Locate every blood parasite and identify its species.
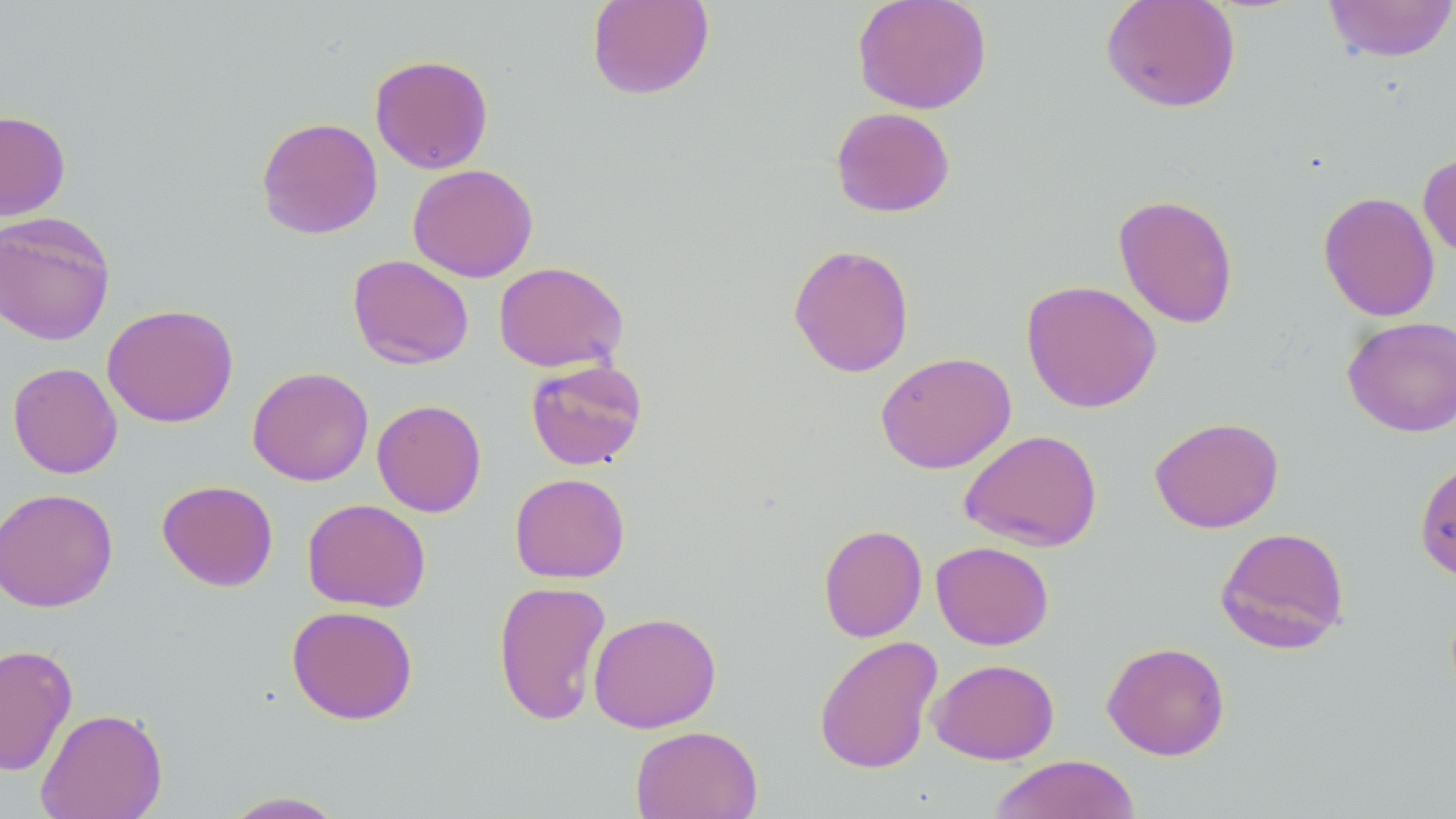

No blood parasites observed.

Summary:
  - Coordinate format: approximate bounding boxes as (x1, y1, x2, y2) in pixels
  - Uninfected red blood cell locations: (586, 0, 715, 100), (851, 0, 993, 115), (1322, 0, 1456, 63), (1100, 1, 1241, 112), (369, 54, 494, 174), (830, 106, 956, 217), (0, 110, 71, 220), (256, 116, 383, 239), (1418, 151, 1456, 261), (408, 163, 538, 282), (1318, 191, 1440, 322), (1113, 193, 1239, 329), (0, 211, 116, 346), (787, 243, 915, 378), (348, 254, 474, 369), (493, 261, 629, 372), (1020, 279, 1162, 413), (102, 303, 239, 428), (1342, 316, 1456, 437), (875, 351, 1017, 474), (525, 359, 648, 470), (7, 362, 123, 479), (247, 367, 374, 486), (371, 399, 487, 517), (1149, 416, 1284, 533), (958, 429, 1104, 552), (1414, 456, 1456, 582), (509, 472, 630, 583), (157, 479, 279, 591), (0, 487, 118, 612), (302, 498, 431, 612), (818, 523, 927, 642), (1215, 526, 1350, 654), (930, 541, 1055, 650), (493, 579, 611, 727), (286, 604, 418, 725), (587, 611, 722, 733), (813, 635, 943, 774), (1102, 641, 1230, 761), (0, 644, 78, 775), (928, 658, 1060, 764), (36, 707, 167, 819), (629, 724, 763, 819), (987, 754, 1142, 819), (219, 790, 350, 818)
  - Slide-level diagnosis: negative for blood parasites
  - Field of view: one of a larger specimen
  - Stain: May-Grünwald-Giemsa
  - Preparation: thin blood smear
  - Image size: 1456×819 pixels
  - Modality: optical microscopy
  - Magnification: 1000x